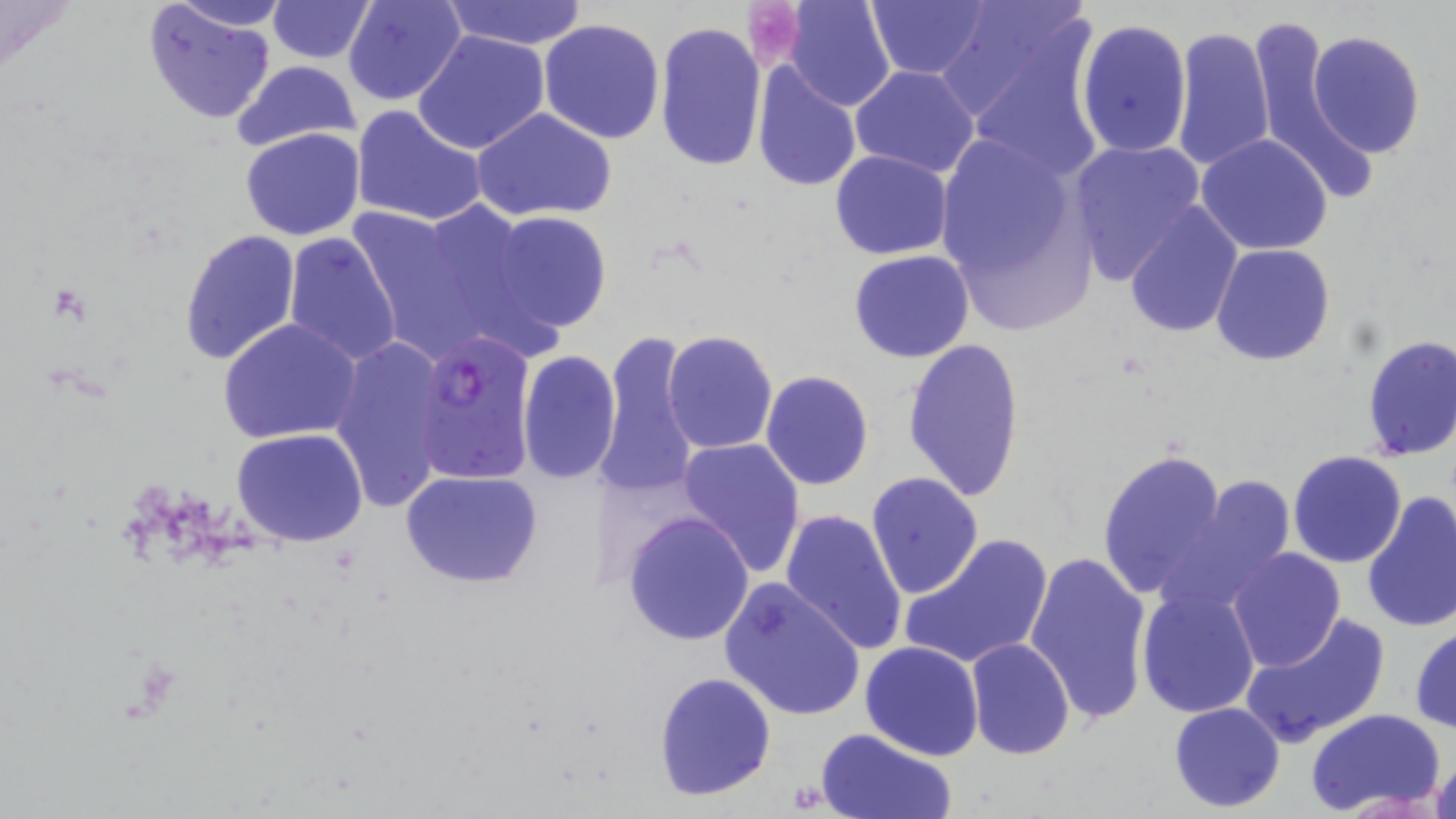

Summary:
  - Coordinate format: approximate bounding boxes as named x1/y1/x2/y2 corners in pixels
  - Uninfected red blood cell locations: (x1=165, y1=0, x2=292, y2=31), (x1=345, y1=0, x2=467, y2=106), (x1=442, y1=0, x2=590, y2=50), (x1=785, y1=0, x2=897, y2=112), (x1=867, y1=0, x2=989, y2=79), (x1=941, y1=0, x2=1098, y2=130), (x1=141, y1=1, x2=276, y2=123), (x1=270, y1=1, x2=374, y2=62), (x1=538, y1=17, x2=665, y2=143), (x1=1074, y1=18, x2=1194, y2=161), (x1=654, y1=21, x2=767, y2=172), (x1=1243, y1=23, x2=1377, y2=192), (x1=1171, y1=25, x2=1275, y2=173), (x1=1307, y1=30, x2=1426, y2=158), (x1=413, y1=31, x2=551, y2=154), (x1=233, y1=58, x2=364, y2=156), (x1=752, y1=64, x2=861, y2=193), (x1=850, y1=65, x2=980, y2=179), (x1=351, y1=105, x2=487, y2=227), (x1=472, y1=108, x2=619, y2=223), (x1=240, y1=127, x2=366, y2=239), (x1=934, y1=132, x2=1093, y2=325), (x1=1195, y1=133, x2=1334, y2=257), (x1=1069, y1=140, x2=1207, y2=285), (x1=830, y1=149, x2=954, y2=259), (x1=353, y1=200, x2=537, y2=354), (x1=1124, y1=203, x2=1245, y2=338), (x1=487, y1=210, x2=613, y2=334), (x1=179, y1=229, x2=302, y2=366), (x1=283, y1=234, x2=403, y2=365), (x1=1211, y1=243, x2=1336, y2=366), (x1=848, y1=250, x2=976, y2=364), (x1=218, y1=318, x2=364, y2=445), (x1=663, y1=330, x2=778, y2=455), (x1=595, y1=331, x2=700, y2=498), (x1=1359, y1=334, x2=1456, y2=462), (x1=902, y1=335, x2=1026, y2=502), (x1=329, y1=337, x2=452, y2=511), (x1=518, y1=351, x2=621, y2=484), (x1=761, y1=370, x2=875, y2=490), (x1=230, y1=428, x2=370, y2=548), (x1=677, y1=439, x2=804, y2=578), (x1=1097, y1=449, x2=1230, y2=602), (x1=1287, y1=451, x2=1407, y2=569), (x1=401, y1=469, x2=545, y2=588), (x1=867, y1=473, x2=984, y2=599), (x1=1163, y1=475, x2=1298, y2=610), (x1=1361, y1=492, x2=1456, y2=634), (x1=781, y1=509, x2=908, y2=657), (x1=623, y1=511, x2=755, y2=646), (x1=901, y1=534, x2=1053, y2=670), (x1=1226, y1=548, x2=1345, y2=670), (x1=1023, y1=549, x2=1151, y2=728), (x1=719, y1=578, x2=865, y2=722), (x1=1135, y1=584, x2=1260, y2=720), (x1=983, y1=607, x2=1125, y2=752), (x1=1240, y1=611, x2=1391, y2=749), (x1=1410, y1=622, x2=1456, y2=734), (x1=964, y1=636, x2=1074, y2=761), (x1=859, y1=640, x2=984, y2=761), (x1=653, y1=671, x2=777, y2=801), (x1=1169, y1=701, x2=1286, y2=813), (x1=1305, y1=707, x2=1447, y2=815), (x1=814, y1=728, x2=956, y2=819), (x1=1429, y1=750, x2=1456, y2=819)
  - Plasmodium falciparum-infected red blood cell locations: (x1=409, y1=330, x2=535, y2=487)
  - Platelet locations: (x1=744, y1=1, x2=803, y2=68)
  - Slide-level diagnosis: Plasmodium falciparum
  - Field of view: one of a larger specimen
  - Preparation: thin blood smear
  - Magnification: 1000x
  - Image size: 1456×819 pixels
  - Modality: light microscopy
  - Stain: May-Grünwald-Giemsa